Outline each Plasmodium ovale-infected red blood cell.
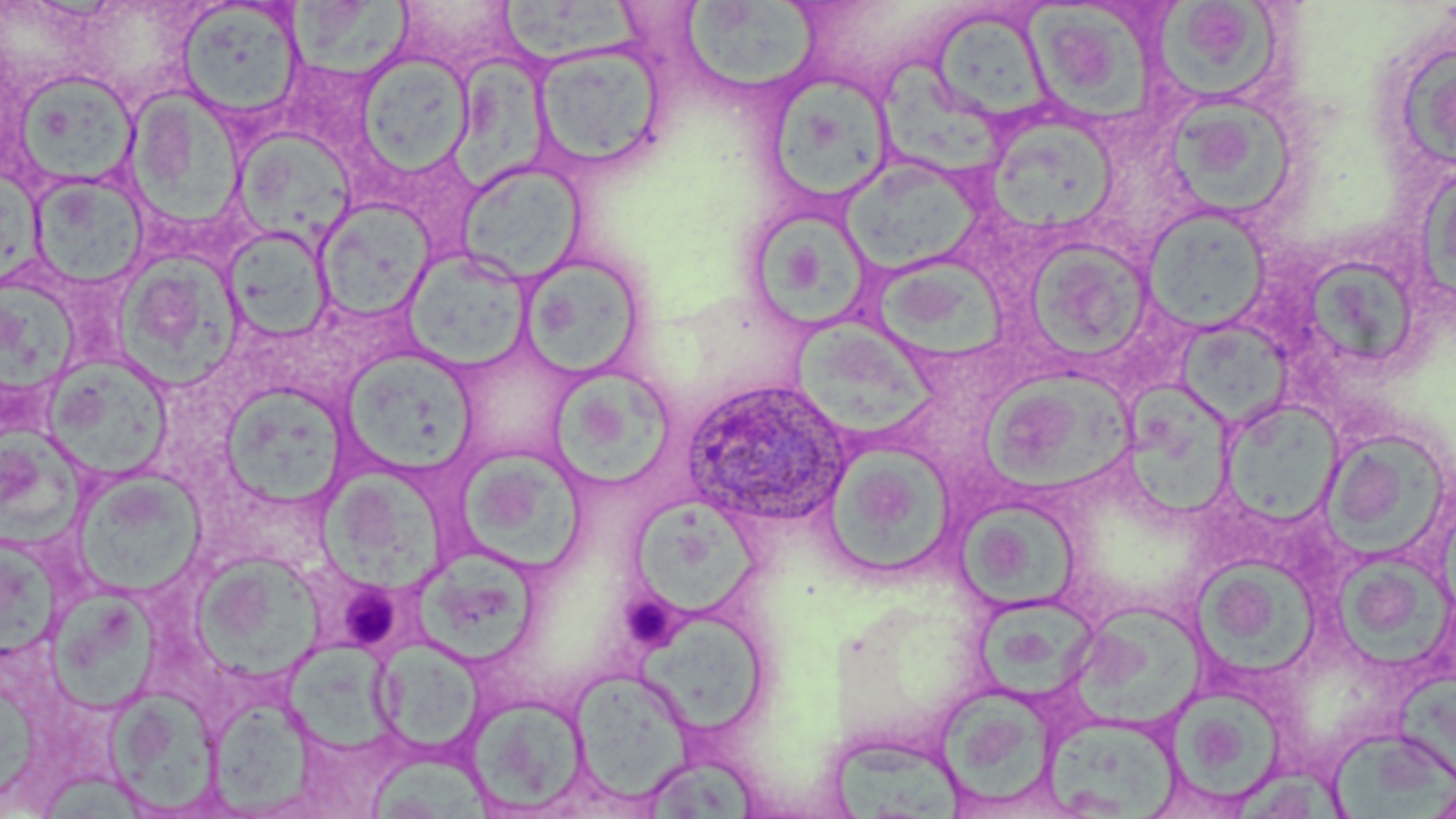

Approximate bounding boxes as (x1,y1)-(x2,y2) corner pairs in pixels.
Plasmodium ovale-infected red blood cells: (682,377)-(854,528).

slide-level diagnosis = Plasmodium ovale
stain = May-Grünwald-Giemsa
preparation = thin blood smear
platelet locations = approximate bounding boxes as (x1,y1)-(x2,y2) corner pairs in pixels: (337,579)-(405,652), (621,596)-(678,647)
image size = 1456×819 pixels
modality = optical microscopy
uninfected red blood cell locations = approximate bounding boxes as (x1,y1)-(x2,y2) corner pairs in pixels: (499,0)-(652,68), (682,1)-(818,93), (177,2)-(305,121), (284,2)-(422,78), (1157,2)-(1284,108), (1024,7)-(1156,129), (933,18)-(1051,117), (532,42)-(668,174), (1401,49)-(1456,167), (452,52)-(551,190), (356,53)-(475,176), (877,58)-(1008,180), (11,69)-(142,190), (771,73)-(896,200), (124,87)-(246,232), (1176,101)-(1292,220), (983,115)-(1121,234), (233,128)-(356,245), (841,156)-(985,276), (1418,158)-(1456,317), (455,160)-(586,285), (29,174)-(151,289), (315,199)-(435,324), (1142,205)-(1273,334), (756,210)-(871,328), (221,226)-(334,344), (1021,236)-(1154,363), (401,249)-(531,370), (874,251)-(1007,364), (518,253)-(647,380), (118,256)-(243,388), (1307,259)-(1414,363), (0,281)-(78,411), (792,316)-(938,442), (1174,316)-(1299,424), (341,348)-(479,472), (43,356)-(172,481), (552,368)-(678,494), (981,369)-(1140,491), (1127,379)-(1237,521), (221,385)-(349,507), (1222,399)-(1342,527), (4,418)-(86,548), (1321,427)-(1450,564), (825,444)-(956,577), (458,450)-(587,573), (70,468)-(208,598), (316,470)-(453,596), (634,501)-(764,621), (955,501)-(1083,613), (0,538)-(68,664), (409,552)-(538,667), (197,557)-(326,682), (1197,560)-(1318,679), (51,585)-(159,711), (972,591)-(1106,695), (1072,599)-(1221,726), (635,619)-(771,733), (276,637)-(413,757), (374,638)-(483,751), (571,672)-(694,802), (1396,672)-(1456,781), (936,684)-(1062,811), (1169,687)-(1290,804), (108,688)-(226,815), (204,695)-(314,816), (468,695)-(592,814), (1046,715)-(1182,818), (1330,727)-(1456,819), (833,737)-(968,819), (642,755)-(764,819), (1239,762)-(1346,819)
field of view = single
magnification = 1000x